Outline platelets.
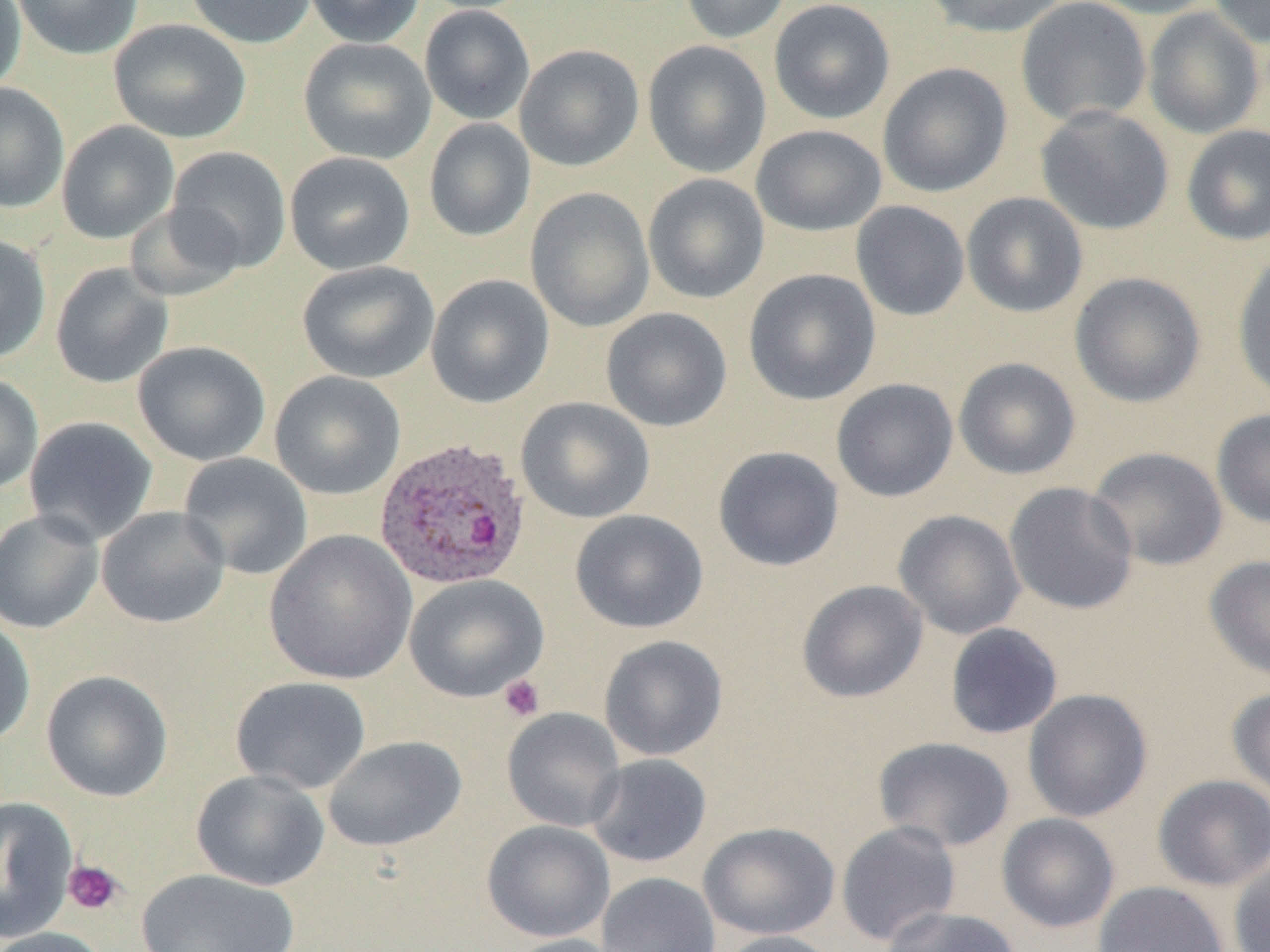

Approximate bounding boxes as (x1, y1, x2, y2) in pixels.
Platelets: (499, 674, 545, 721), (63, 859, 124, 915).

Summary:
  - Uninfected red blood cell locations: (0, 0, 27, 94), (10, 0, 144, 60), (185, 0, 317, 49), (303, 0, 426, 48), (679, 0, 792, 44), (920, 0, 1070, 38), (1016, 0, 1152, 127), (1082, 0, 1220, 19), (1207, 0, 1270, 48), (768, 1, 895, 124), (419, 4, 535, 125), (1142, 7, 1265, 139), (108, 18, 251, 144), (298, 37, 436, 164), (642, 40, 771, 178), (514, 44, 644, 172), (878, 62, 1012, 198), (0, 82, 70, 213), (1035, 105, 1174, 236), (423, 118, 536, 241), (57, 121, 179, 244), (750, 124, 887, 237), (1181, 124, 1270, 246), (166, 145, 291, 273), (284, 151, 415, 275), (643, 173, 770, 304), (525, 187, 655, 332), (961, 192, 1088, 318), (850, 201, 970, 321), (124, 203, 246, 301), (0, 234, 51, 364), (1232, 253, 1270, 403), (297, 260, 440, 384), (49, 263, 173, 389), (743, 268, 881, 406), (1069, 272, 1206, 408), (425, 273, 555, 408), (601, 307, 732, 432), (132, 341, 271, 466), (953, 357, 1081, 480), (269, 370, 406, 500), (0, 372, 44, 494), (831, 378, 959, 502), (515, 396, 655, 524), (1211, 408, 1270, 529), (24, 415, 158, 545), (712, 446, 844, 572), (1086, 446, 1229, 571), (177, 452, 313, 580), (1004, 482, 1139, 614), (96, 506, 230, 629), (0, 508, 105, 634), (570, 509, 708, 634), (893, 509, 1026, 640), (264, 529, 417, 685), (1205, 555, 1270, 682), (404, 575, 548, 702), (796, 579, 929, 703), (0, 615, 36, 748), (945, 623, 1063, 739), (598, 634, 728, 761), (41, 669, 173, 802), (229, 676, 372, 794), (1227, 685, 1270, 801), (1023, 689, 1153, 823), (502, 707, 626, 832), (322, 735, 466, 852), (873, 736, 1016, 852), (586, 753, 712, 868), (190, 769, 329, 891), (1152, 774, 1270, 892), (0, 796, 77, 943), (996, 813, 1120, 934), (481, 820, 615, 942), (836, 821, 961, 947), (698, 822, 840, 940), (1228, 857, 1270, 952), (136, 868, 300, 952), (596, 872, 720, 952), (1092, 881, 1229, 952), (878, 905, 1024, 952), (0, 926, 112, 952), (715, 930, 842, 952), (500, 934, 629, 952)
  - Plasmodium ovale-infected red blood cell locations: (373, 436, 531, 591)
  - Slide-level diagnosis: Plasmodium ovale
  - Field of view: one of a larger specimen
  - Modality: optical microscopy
  - Magnification: 1000x
  - Image size: 1270×952 pixels
  - Preparation: thin blood film